State which parasite is depicted.
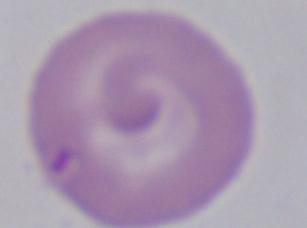

Babesia.

magnification = 1000x
modality = micrograph